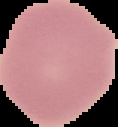
Summary:
  - Result: no malaria parasites detected
  - Preparation: thin blood film
  - Image type: segmented cell region on a black background
  - Image size: 118×127 pixels